Classify this cell by malaria status.
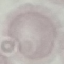
Uninfected.

Cell patch, automatically extracted from a larger field of view and resized to 64 × 64 pixels. Giemsa-stained preparation. Thin blood film. Acquired by smartphone through the microscope eyepiece.